Report the malaria status of this cell.
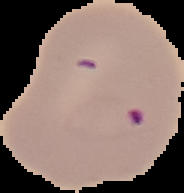
Parasitized.

image size = 184×193 pixels
preparation = thin blood smear
image type = segmented cell region on a black background